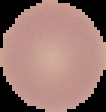
image_size: 106×112 pixels
image_type: cell region segmented out of the field of view; surrounding area masked to black
result: no malaria parasites detected
preparation: thin blood smear